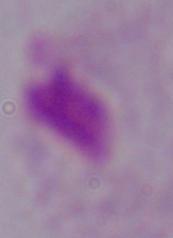
Micrograph. A trichomonad is seen. Captured at 1000x magnification.